Assess this cell for malaria.
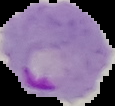
Parasitized.

Summary:
  - Image size: 115×106 pixels
  - Image type: cell region segmented out of the field of view; surrounding area masked to black
  - Preparation: thin blood smear